Identify the parasite.
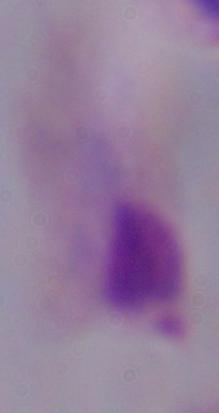
This is a trichomonad.

Summary:
  - Modality: micrograph
  - Magnification: 1000x